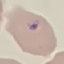
Summary:
  - Malaria status: parasitized
  - Image type: automatically extracted cell patch, resized to 64 × 64 pixels
  - Stain: Giemsa
  - Capture: smartphone through the microscope eyepiece
  - Preparation: thin smear